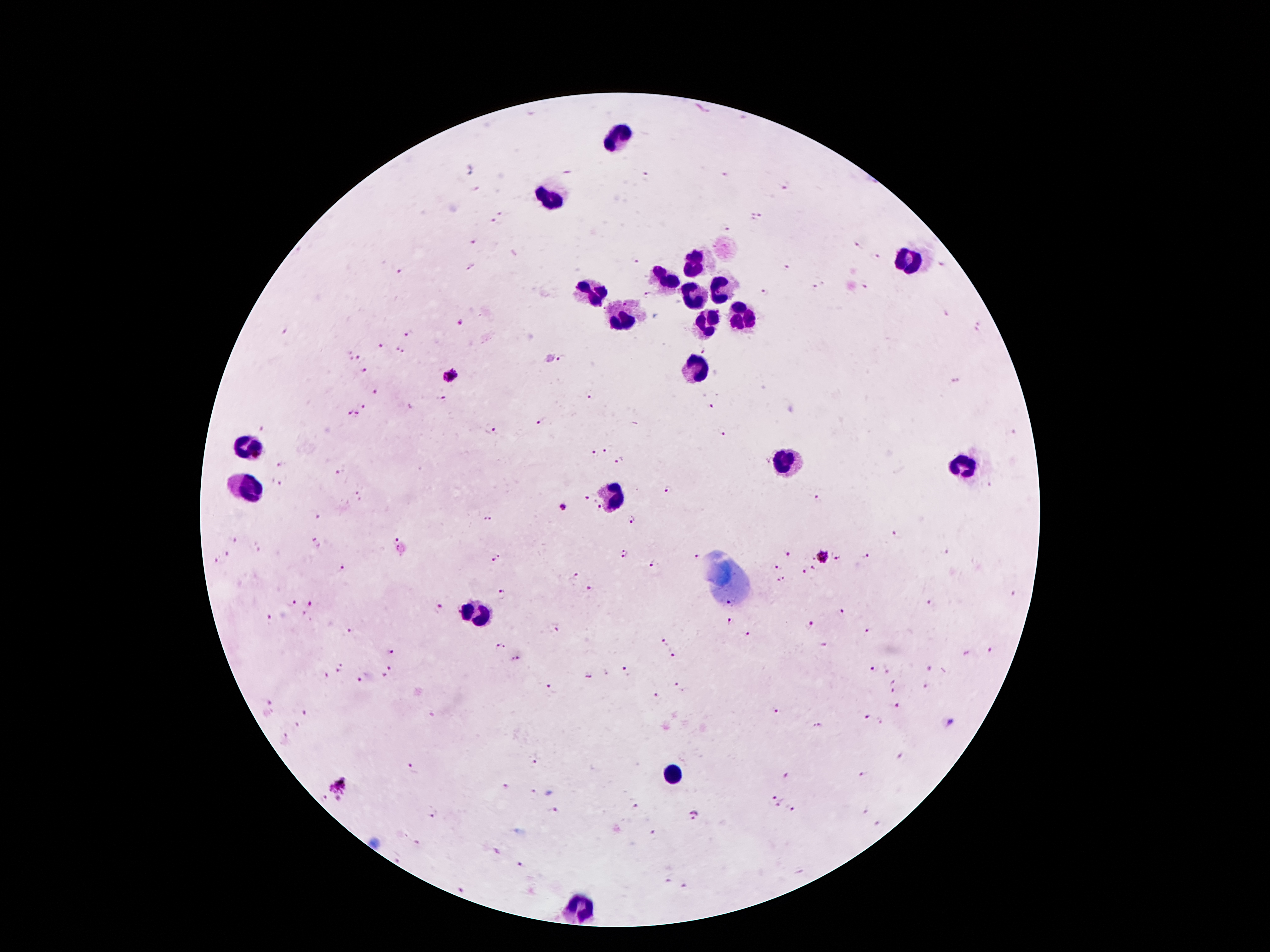

Approximate centers as {x, y} in pixels. Plasmodium parasite locations: {724, 173}, {645, 174}, {786, 187}, {503, 214}, {761, 216}, {753, 217}, {493, 222}, {729, 228}, {474, 241}, {858, 244}, {879, 257}, {636, 263}, {941, 265}, {470, 267}, {787, 267}, {398, 271}, {815, 287}, {865, 288}, {764, 292}, {648, 295}, {945, 313}, {460, 323}, {978, 326}, {283, 332}, {409, 333}, {383, 347}, {703, 351}, {399, 352}, {359, 358}, {562, 358}, {363, 370}, {450, 376}, {956, 382}, {375, 392}, {442, 396}, {591, 396}, {712, 405}, {364, 406}, {348, 414}, {356, 415}, {542, 421}, {489, 431}, {720, 431}, {607, 451}, {594, 454}, {620, 461}, {281, 464}, {339, 474}, {277, 485}, {669, 489}, {357, 493}, {587, 498}, {818, 499}, {563, 508}, {599, 508}, {316, 515}, {486, 518}, {631, 520}, {894, 535}, {395, 539}, {232, 541}, {315, 543}, {623, 552}, {787, 552}, {228, 553}, {947, 553}, {696, 556}, {866, 556}, {822, 558}, {839, 559}, {215, 560}, {496, 560}, {653, 563}, {775, 567}, {343, 569}, {812, 569}, {804, 573}, {575, 576}, {781, 580}, {590, 589}, {503, 591}, {1014, 594}, {292, 603}, {931, 603}, {310, 604}, {439, 607}, {842, 611}, {270, 616}, {730, 621}, {809, 626}, {556, 628}, {348, 629}, {868, 631}, {749, 634}, {662, 642}, {825, 645}, {500, 646}, {992, 650}, {391, 653}, {674, 654}, {518, 659}, {873, 667}, {341, 668}, {392, 668}, {931, 668}, {627, 672}, {385, 674}, {325, 675}, {589, 676}, {360, 680}, {892, 681}, {676, 684}, {549, 685}, {926, 686}, {892, 691}, {656, 696}, {269, 703}, {898, 706}, {775, 710}, {306, 712}, {867, 717}, {298, 726}, {816, 726}, {286, 736}, {534, 763}, {411, 767}, {864, 773}, {786, 775}, {340, 788}, {505, 788}, {532, 793}, {774, 796}, {324, 800}, {638, 805}, {778, 805}, {792, 809}, {555, 810}, {865, 810}, {693, 815}, {433, 816}, {879, 824}, {653, 834}, {521, 864}, {667, 881}, {684, 887}, {462, 890}. Leukocyte locations: {619, 137}, {552, 196}, {909, 261}, {692, 263}, {662, 278}, {720, 285}, {593, 291}, {695, 295}, {743, 311}, {621, 314}, {708, 319}, {697, 369}, {245, 447}, {787, 459}, {964, 465}, {250, 488}, {611, 497}, {474, 612}, {674, 772}, {580, 907}. One field from this slide. Thick blood smear. Smartphone photograph taken through the microscope eyepiece. Patient malaria status: infected with Plasmodium falciparum. Giemsa stain. 100x magnification. Image is 1270×952 pixels.